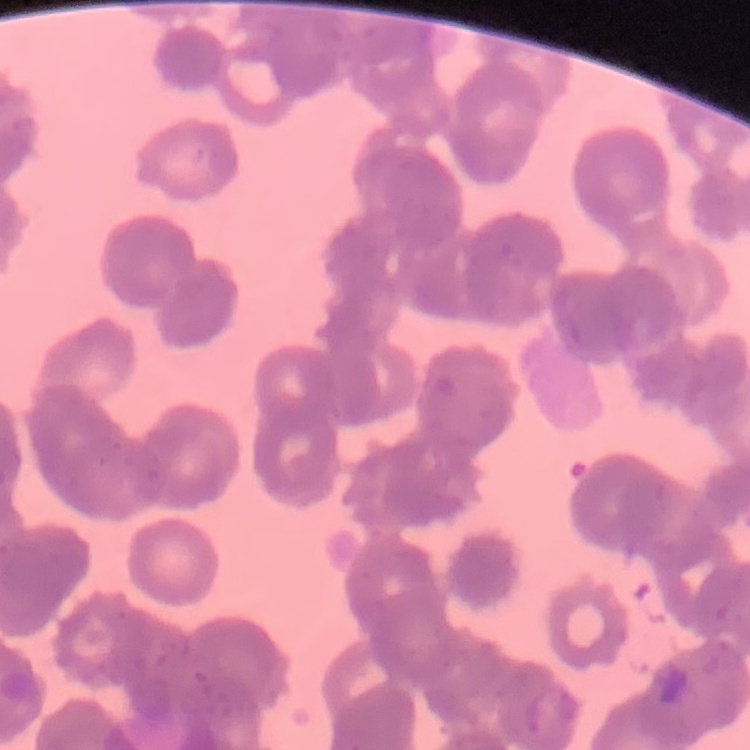 The red blood cells exhibit rouleaux formation. Thin blood smear. Field's or Giemsa stain. One tile cut from a larger photomicrograph.